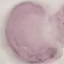 Malaria status: uninfected. Cell patch, automatically extracted from a larger field of view and resized to 64 × 64 pixels. Acquired by smartphone through the microscope eyepiece. Giemsa stain. Thin blood smear.